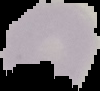

Summary:
  - Result: negative for Plasmodium parasites
  - Preparation: thin blood film
  - Image size: 100×91 pixels
  - Image type: segmented cell region with the area outside set to black